Outline platelets.
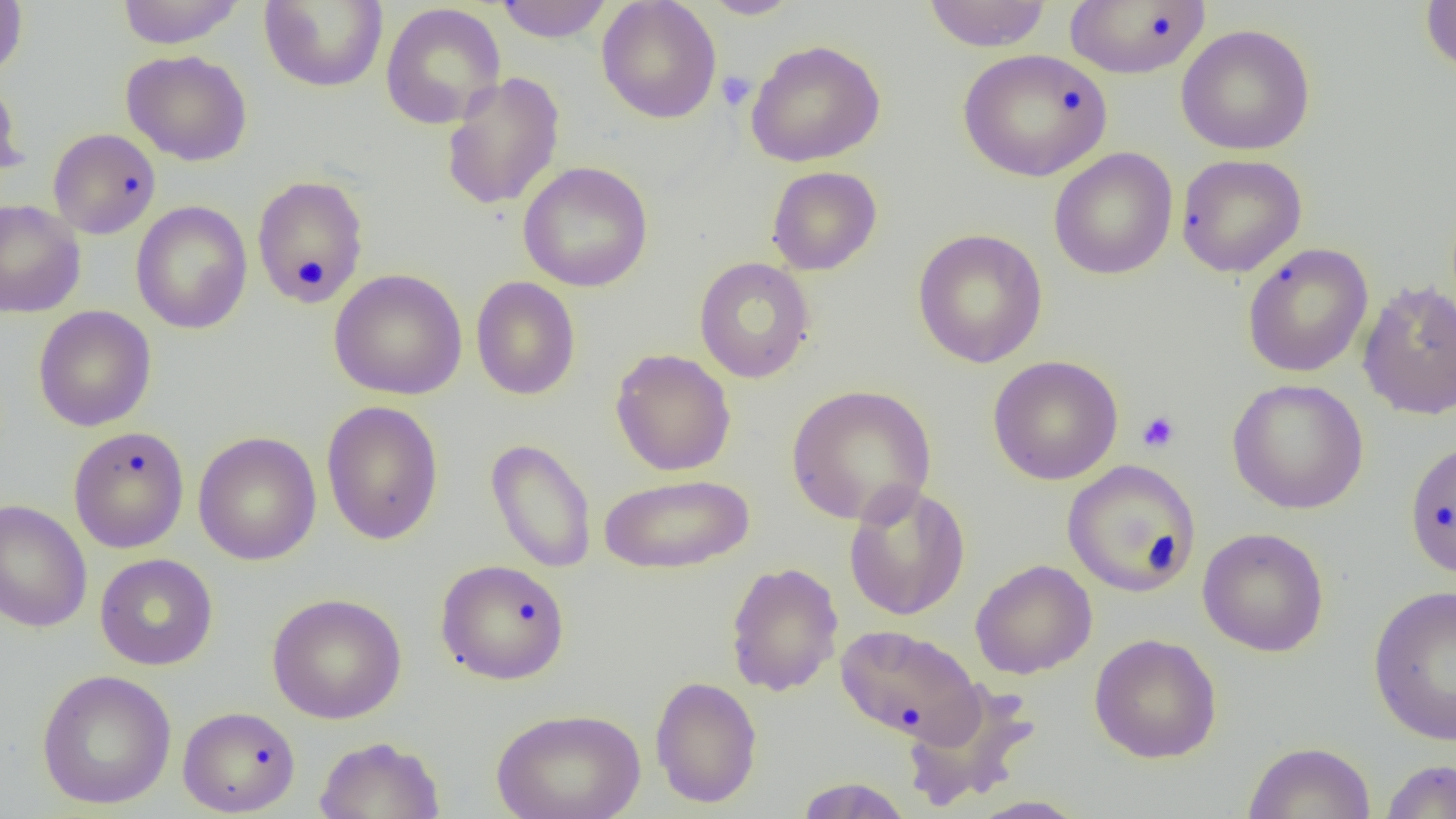
Approximate bounding boxes as [x1, y1, x2, y2] in pixels.
Platelets: [716, 70, 756, 111], [1136, 410, 1181, 453].

Summary:
  - Uninfected red blood cell locations: [0, 0, 28, 80], [116, 0, 245, 48], [495, 0, 614, 42], [597, 0, 721, 124], [700, 0, 803, 19], [921, 0, 1053, 52], [259, 1, 389, 92], [1064, 1, 1212, 78], [1420, 1, 1455, 79], [380, 3, 506, 129], [1175, 24, 1316, 155], [745, 38, 885, 167], [957, 48, 1113, 182], [120, 49, 253, 167], [441, 71, 565, 211], [0, 76, 26, 183], [48, 128, 161, 239], [1048, 147, 1178, 280], [1176, 153, 1307, 277], [518, 160, 653, 292], [766, 166, 882, 275], [251, 175, 369, 309], [0, 199, 86, 318], [131, 200, 252, 334], [912, 228, 1048, 368], [1242, 243, 1374, 378], [694, 257, 815, 383], [329, 268, 467, 400], [470, 276, 581, 401], [1357, 279, 1456, 420], [33, 305, 157, 431], [610, 348, 736, 476], [987, 355, 1124, 485], [1227, 378, 1368, 515], [786, 384, 937, 526], [321, 400, 444, 545], [68, 425, 190, 553], [193, 431, 322, 566], [485, 437, 597, 573], [1403, 438, 1456, 579], [1062, 459, 1201, 597], [598, 473, 755, 575], [843, 481, 970, 621], [0, 499, 92, 633], [1198, 527, 1329, 657], [95, 553, 218, 670], [435, 559, 571, 685], [970, 559, 1098, 680], [724, 561, 844, 697], [1367, 584, 1456, 747], [267, 592, 407, 724], [835, 624, 984, 745], [1089, 633, 1222, 763], [36, 668, 177, 810], [649, 675, 763, 808], [901, 680, 1042, 811], [178, 705, 301, 817], [491, 707, 646, 819], [314, 736, 446, 819], [1241, 741, 1377, 819], [1379, 759, 1456, 818], [793, 777, 914, 818], [966, 795, 1090, 818]
  - Slide-level diagnosis: no evidence of blood parasites
  - Preparation: thin blood smear
  - Magnification: 1000x
  - Field of view: one of a larger specimen
  - Modality: light microscopy
  - Image size: 1456×819 pixels